Classify this cell by malaria status.
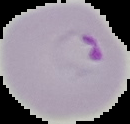
It is parasitized.

Summary:
  - Image size: 130×124 pixels
  - Image type: cell region segmented out of the field of view; surrounding area masked to black
  - Preparation: thin blood film